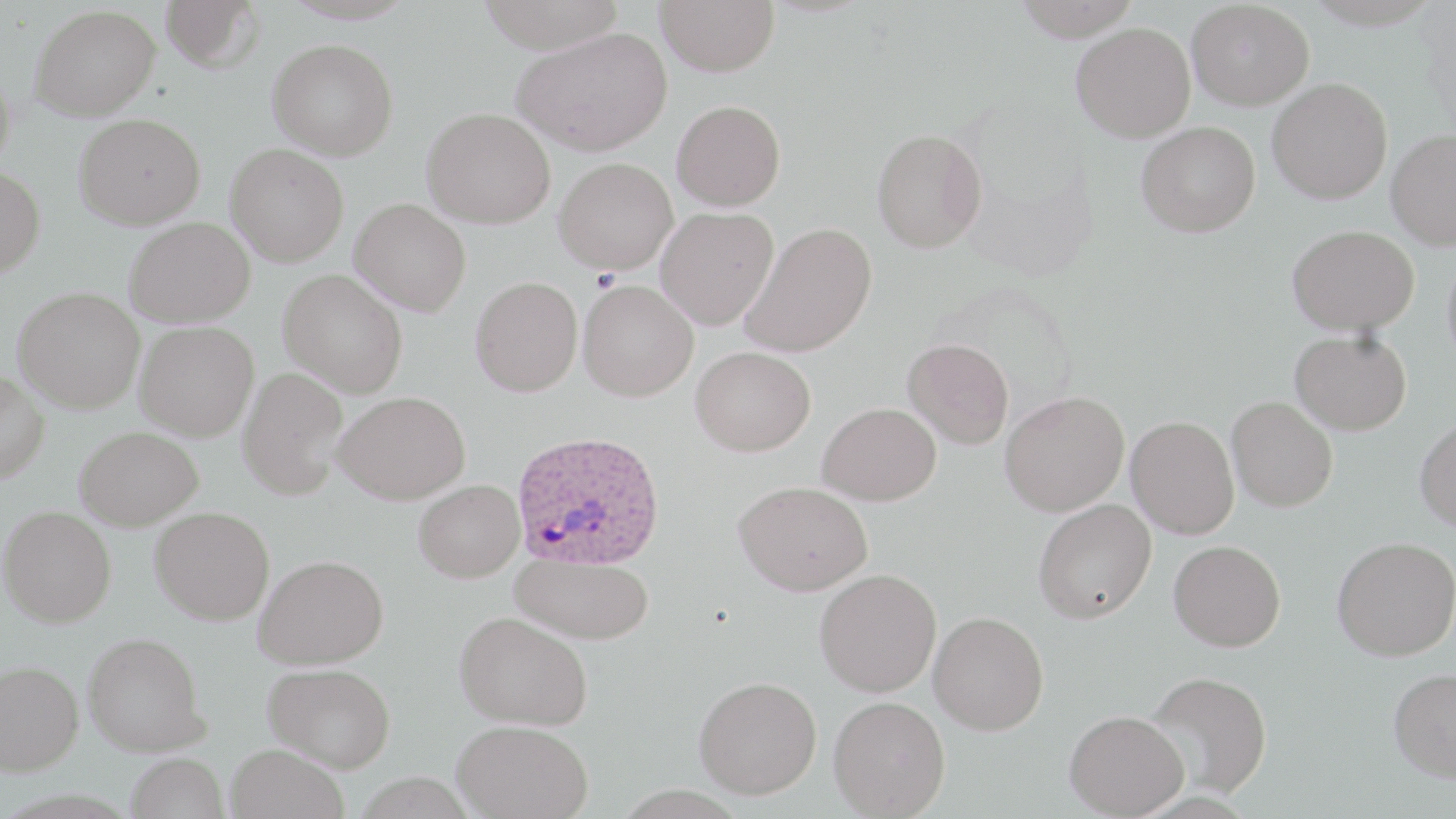

Approximate bounding boxes as (x1, y1, x2, y2) in pixels. Plasmodium ovale-infected red blood cell locations: (511, 429, 667, 571). Platelet locations: (590, 268, 621, 293). Uninfected red blood cell locations: (160, 0, 266, 73), (475, 0, 627, 53), (655, 0, 779, 76), (1013, 0, 1142, 41), (1186, 1, 1314, 110), (30, 4, 160, 121), (1071, 22, 1196, 142), (512, 26, 673, 156), (267, 38, 398, 161), (0, 61, 16, 175), (1267, 77, 1392, 204), (672, 99, 786, 211), (421, 107, 556, 228), (73, 112, 205, 230), (1136, 121, 1260, 237), (871, 128, 987, 253), (1386, 129, 1456, 249), (225, 143, 348, 266), (554, 157, 678, 275), (0, 165, 46, 278), (350, 198, 471, 316), (655, 207, 779, 329), (124, 216, 255, 327), (740, 222, 877, 358), (1287, 224, 1419, 336), (1442, 244, 1456, 373), (278, 269, 408, 397), (470, 276, 583, 396), (578, 280, 698, 401), (12, 286, 145, 414), (134, 321, 258, 441), (1289, 330, 1411, 435), (903, 338, 1014, 449), (691, 346, 816, 456), (237, 367, 347, 499), (0, 369, 49, 484), (999, 390, 1129, 516), (334, 391, 470, 504), (1226, 396, 1338, 512), (817, 401, 941, 506), (1126, 416, 1239, 539), (1415, 417, 1456, 532), (75, 426, 203, 531), (413, 480, 524, 582), (734, 480, 873, 595), (1033, 499, 1156, 624), (1, 505, 116, 627), (150, 506, 274, 625), (1332, 537, 1456, 660), (1169, 540, 1285, 651), (511, 552, 653, 644), (254, 554, 389, 669), (814, 569, 942, 697), (454, 610, 592, 730), (928, 611, 1048, 735), (83, 631, 209, 756), (0, 660, 83, 775), (263, 662, 396, 772), (1387, 667, 1456, 782), (1144, 670, 1273, 799), (693, 676, 821, 798), (828, 695, 950, 818), (1064, 709, 1188, 818), (452, 719, 593, 818), (225, 743, 349, 819), (125, 752, 229, 819). Slide-level diagnosis: Plasmodium ovale. 1000x magnification. Light microscopy. Image is 1456×819 pixels. May-Grünwald-Giemsa stain. Thin blood film. Single field of view.